Name the blood parasite species.
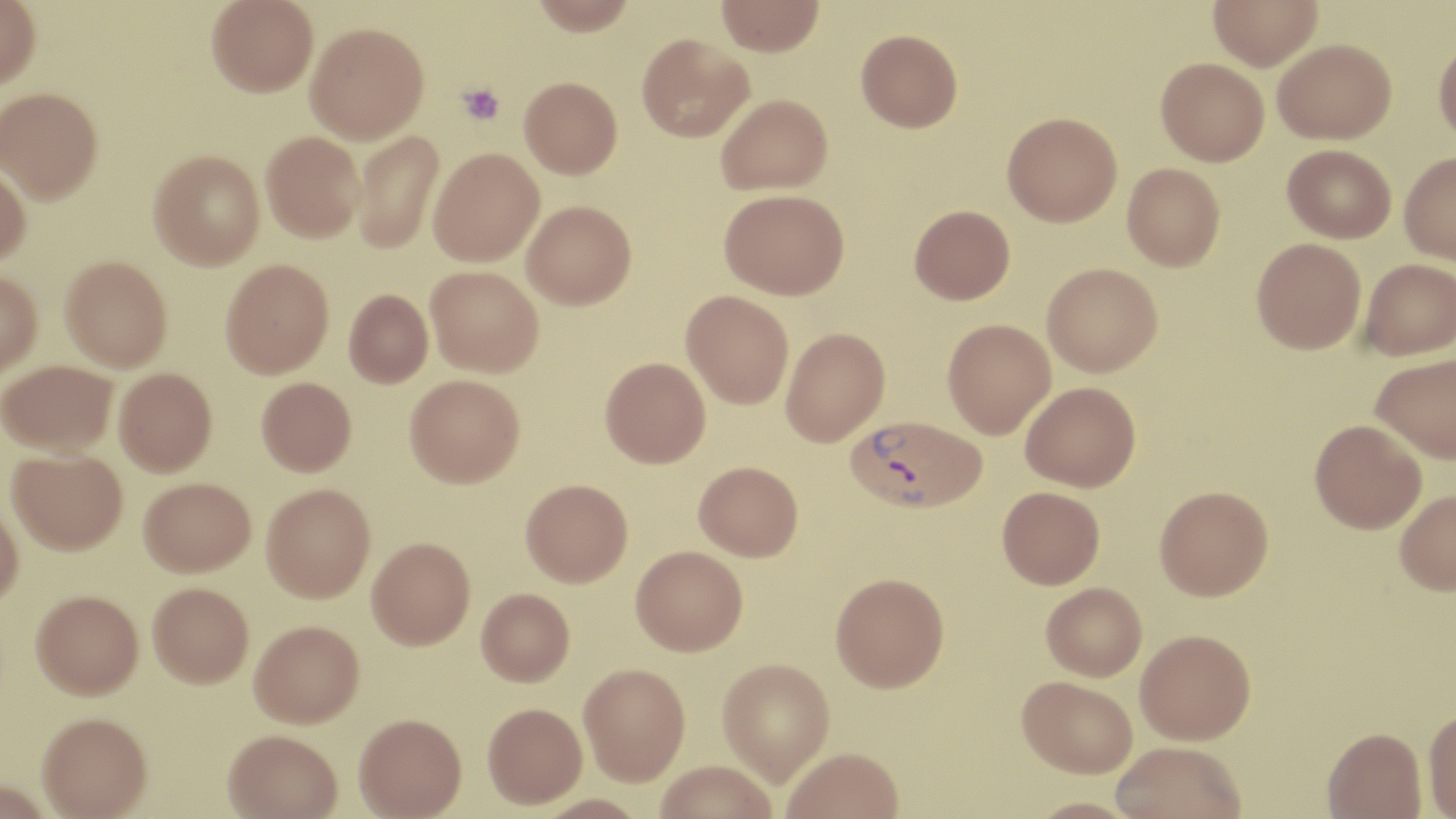

Plasmodium vivax.

image size = 1456×819 pixels
preparation = thin blood film
uninfected red blood cell locations = approximate bounding boxes as (x1, y1, x2, y2) in pixels: (0, 0, 41, 88), (206, 0, 318, 97), (529, 0, 637, 36), (716, 0, 825, 56), (1208, 0, 1323, 70), (306, 22, 429, 143), (856, 28, 962, 132), (636, 33, 753, 142), (1434, 36, 1456, 145), (1273, 38, 1396, 143), (1156, 57, 1269, 165), (519, 76, 622, 178), (0, 87, 103, 202), (716, 93, 832, 195), (1002, 111, 1122, 226), (351, 130, 444, 254), (261, 131, 364, 242), (1282, 144, 1396, 242), (428, 147, 544, 266), (149, 149, 264, 270), (1399, 152, 1456, 264), (0, 162, 31, 265), (1122, 163, 1225, 271), (719, 188, 849, 299), (522, 201, 636, 309), (909, 204, 1015, 304), (1251, 237, 1366, 354), (60, 256, 172, 371), (1360, 258, 1456, 360), (220, 259, 334, 377), (1042, 262, 1163, 376), (425, 265, 543, 376), (0, 269, 42, 378), (344, 289, 433, 387), (680, 290, 794, 409), (942, 319, 1055, 439), (781, 327, 890, 446), (1371, 354, 1456, 462), (600, 357, 711, 468), (0, 360, 117, 455), (114, 367, 217, 476), (405, 374, 524, 487), (256, 376, 356, 476), (1021, 381, 1141, 491), (1310, 419, 1427, 533), (7, 448, 128, 554), (694, 461, 803, 560), (139, 477, 256, 577), (521, 478, 633, 586), (262, 483, 376, 602), (1154, 485, 1273, 600), (997, 486, 1105, 588), (1394, 489, 1456, 595), (0, 497, 24, 607), (367, 536, 475, 649), (630, 545, 748, 655), (830, 572, 949, 691), (148, 582, 254, 687), (1041, 582, 1147, 681), (476, 588, 574, 685), (31, 589, 143, 699), (249, 619, 364, 727), (1135, 629, 1255, 744), (717, 659, 834, 785), (579, 663, 690, 787), (1017, 675, 1137, 777), (482, 703, 588, 810), (1423, 707, 1456, 818), (37, 711, 153, 818), (354, 714, 467, 819), (1322, 727, 1426, 819), (223, 728, 342, 819), (1111, 741, 1246, 819), (782, 748, 904, 819), (655, 762, 778, 819), (1023, 798, 1145, 819)
Plasmodium vivax-infected red blood cell locations = approximate bounding boxes as (x1, y1, x2, y2) in pixels: (846, 415, 986, 513)
platelet locations = approximate bounding boxes as (x1, y1, x2, y2) in pixels: (456, 82, 506, 125)
modality = light microscopy
magnification = 1000x
field of view = one of a larger specimen
stain = May-Grünwald-Giemsa